Describe the morphology of the red blood cells.
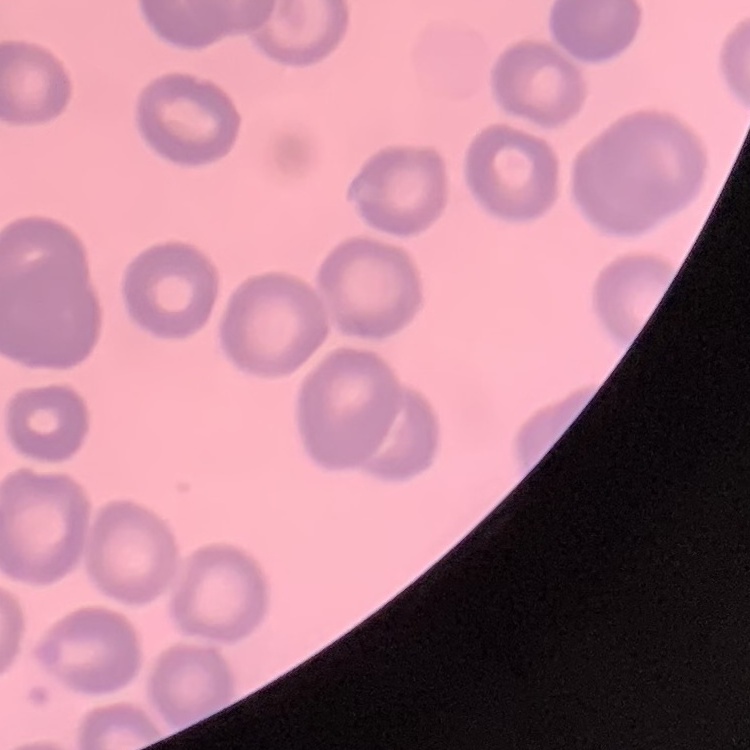

They show no rouleaux formation.

Thin peripheral smear. Square crop of a larger photomicrograph. Stained with either Field's or Giemsa.